Describe the morphology of the erythrocytes.
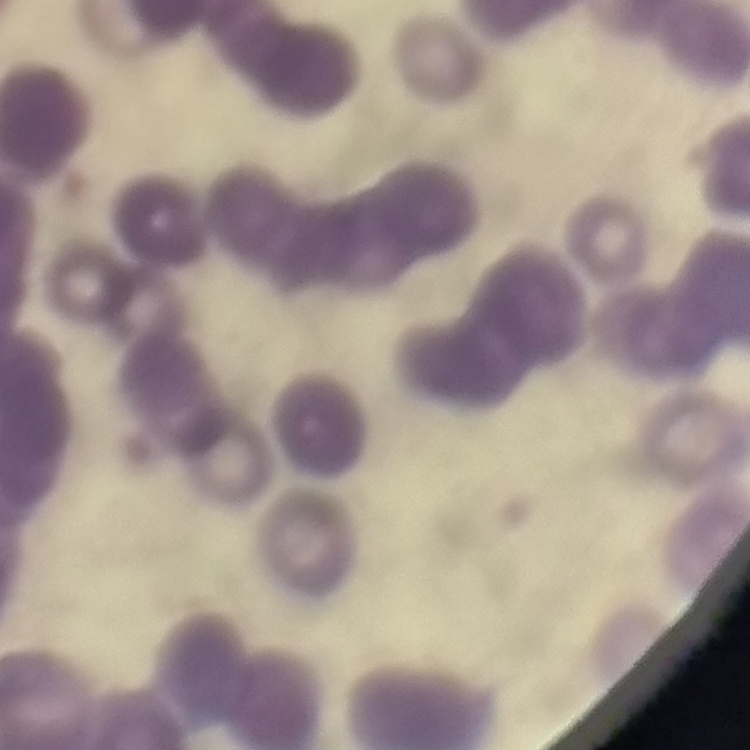
Rouleaux formation.

image type = one tile cut from a larger photomicrograph
stain = Field's or Giemsa
preparation = thin peripheral smear